Locate every blood parasite and identify its species.
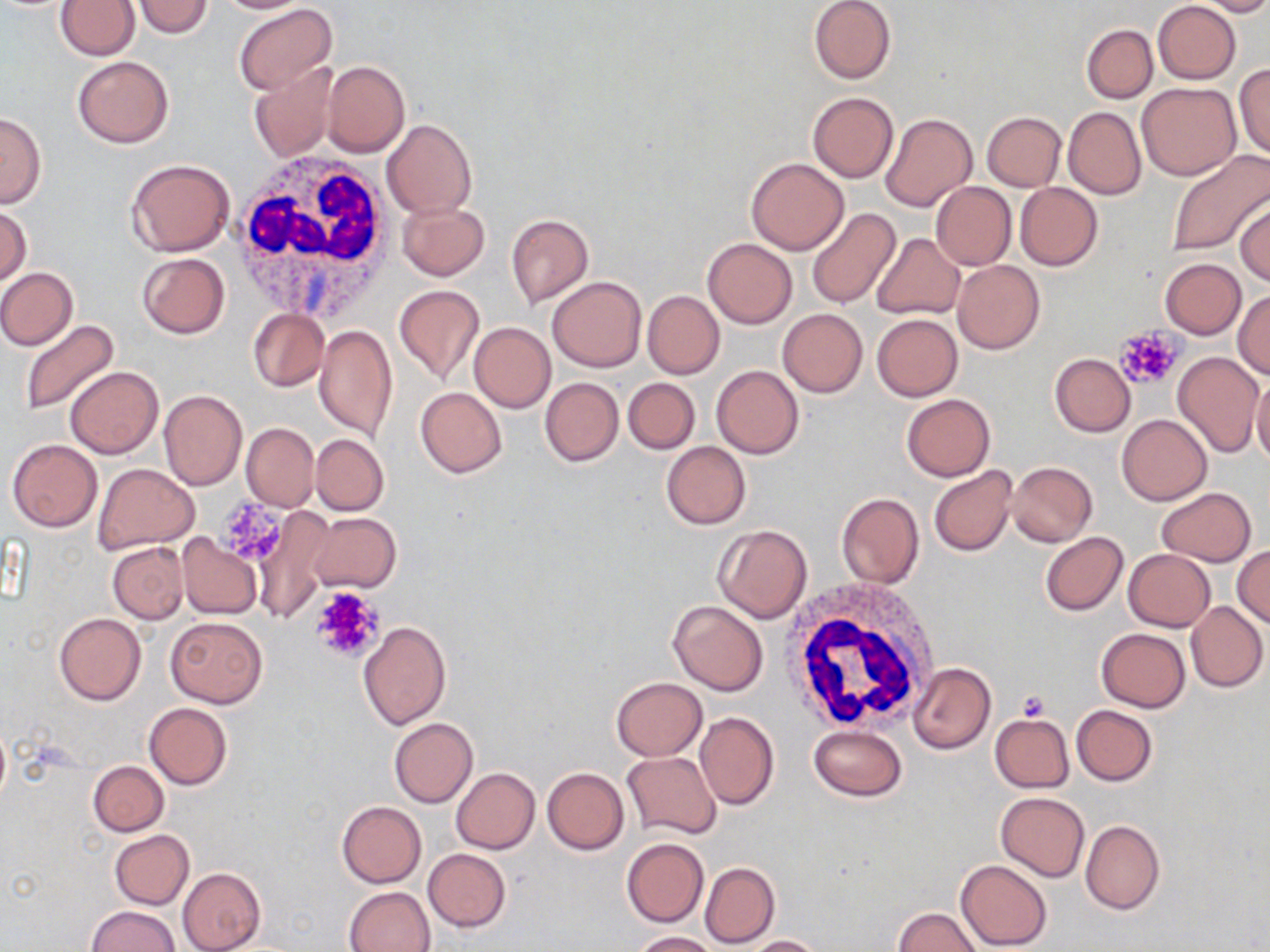
No blood parasites observed.

slide_level_diagnosis: negative for blood parasites
magnification: 1000x
preparation: thin blood smear
stain: May-Grünwald-Giemsa
platelet_locations: 'approximate bounding boxes as [x1, y1, x2, y2] in pixels: [1114, 326, 1184, 391], [217, 498, 291, 566], [308, 585, 387, 664], [1017, 691, 1050, 721]'
image_size: 1270×952 pixels
white_blood_cell_locations: 'approximate bounding boxes as [x1, y1, x2, y2] in pixels: [232, 150, 394, 321], [778, 579, 945, 736]'
uninfected_red_blood_cell_locations: 'approximate bounding boxes as [x1, y1, x2, y2] in pixels: [131, 0, 212, 39], [211, 0, 315, 14], [1193, 0, 1270, 16], [55, 1, 140, 60], [808, 1, 895, 85], [1152, 1, 1241, 84], [234, 4, 336, 95], [1082, 24, 1157, 103], [72, 54, 174, 148], [321, 60, 410, 156], [1233, 62, 1270, 162], [247, 64, 337, 161], [1136, 82, 1241, 180], [807, 92, 898, 184], [1063, 107, 1146, 200], [981, 111, 1066, 191], [0, 112, 46, 209], [880, 113, 977, 212], [381, 119, 478, 218], [1164, 150, 1270, 257], [746, 157, 849, 254], [126, 158, 236, 256], [930, 181, 1015, 271], [1213, 182, 1270, 282], [1014, 183, 1103, 271], [1234, 199, 1269, 288], [398, 201, 489, 280], [0, 206, 31, 288], [805, 208, 901, 309], [506, 214, 594, 307], [870, 233, 964, 320], [703, 239, 797, 328], [137, 253, 230, 338], [1159, 258, 1246, 339], [952, 260, 1044, 354], [0, 267, 77, 350], [547, 274, 647, 372], [393, 286, 486, 387], [1232, 290, 1270, 380], [643, 291, 724, 379], [777, 308, 868, 398], [248, 309, 328, 391], [871, 313, 963, 401], [19, 319, 120, 416], [469, 322, 555, 412], [314, 325, 397, 443], [1173, 352, 1263, 457], [1049, 353, 1135, 437], [711, 365, 804, 458], [65, 367, 163, 458], [1251, 375, 1270, 470], [539, 376, 623, 467], [623, 378, 700, 454], [416, 387, 506, 478], [158, 390, 246, 490], [900, 394, 996, 481], [1116, 414, 1211, 505], [241, 422, 319, 511], [310, 433, 389, 516], [7, 438, 102, 533], [660, 440, 750, 530], [1007, 461, 1097, 547], [92, 463, 199, 553], [929, 466, 1017, 556], [1156, 487, 1256, 566], [836, 493, 924, 591], [254, 506, 337, 621], [308, 513, 400, 594], [714, 524, 813, 623], [1039, 532, 1128, 616], [177, 534, 262, 619], [108, 542, 188, 623], [1232, 544, 1270, 629], [1124, 549, 1215, 631], [668, 599, 768, 696], [1185, 600, 1267, 692], [53, 613, 145, 705], [165, 616, 268, 708], [358, 621, 451, 730], [1096, 627, 1190, 712], [908, 662, 995, 754], [611, 677, 707, 760], [144, 703, 231, 789], [1072, 705, 1156, 785], [695, 712, 779, 810], [990, 714, 1075, 792], [389, 718, 478, 807], [810, 724, 906, 802], [622, 750, 722, 839], [88, 761, 169, 836], [542, 767, 629, 854], [451, 768, 539, 853], [995, 792, 1090, 881], [336, 801, 426, 888], [1080, 819, 1164, 915], [108, 829, 194, 909], [622, 838, 709, 928], [423, 848, 511, 932], [956, 859, 1052, 951], [700, 861, 780, 949], [178, 867, 266, 951], [344, 886, 434, 952], [87, 905, 178, 952], [893, 907, 983, 952], [630, 931, 720, 951], [744, 935, 826, 952]'
modality: optical microscopy
field_of_view: one of a larger specimen